State which parasite is depicted.
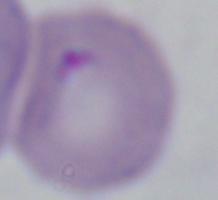
Babesia.

modality = micrograph
magnification = 1000x